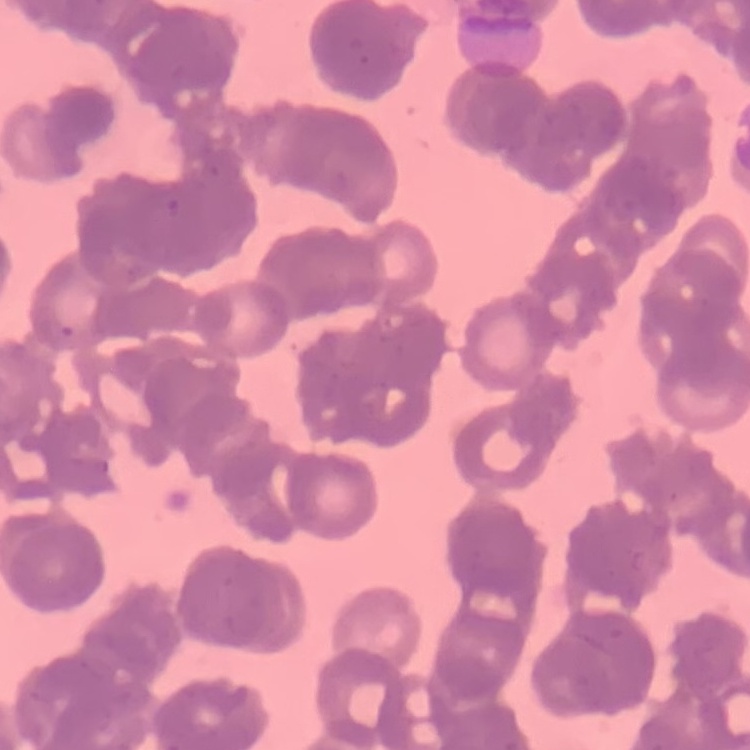

red blood cell morphology = rouleaux formation
preparation = thin blood smear
image type = square crop of a larger photomicrograph
stain = Field's or Giemsa